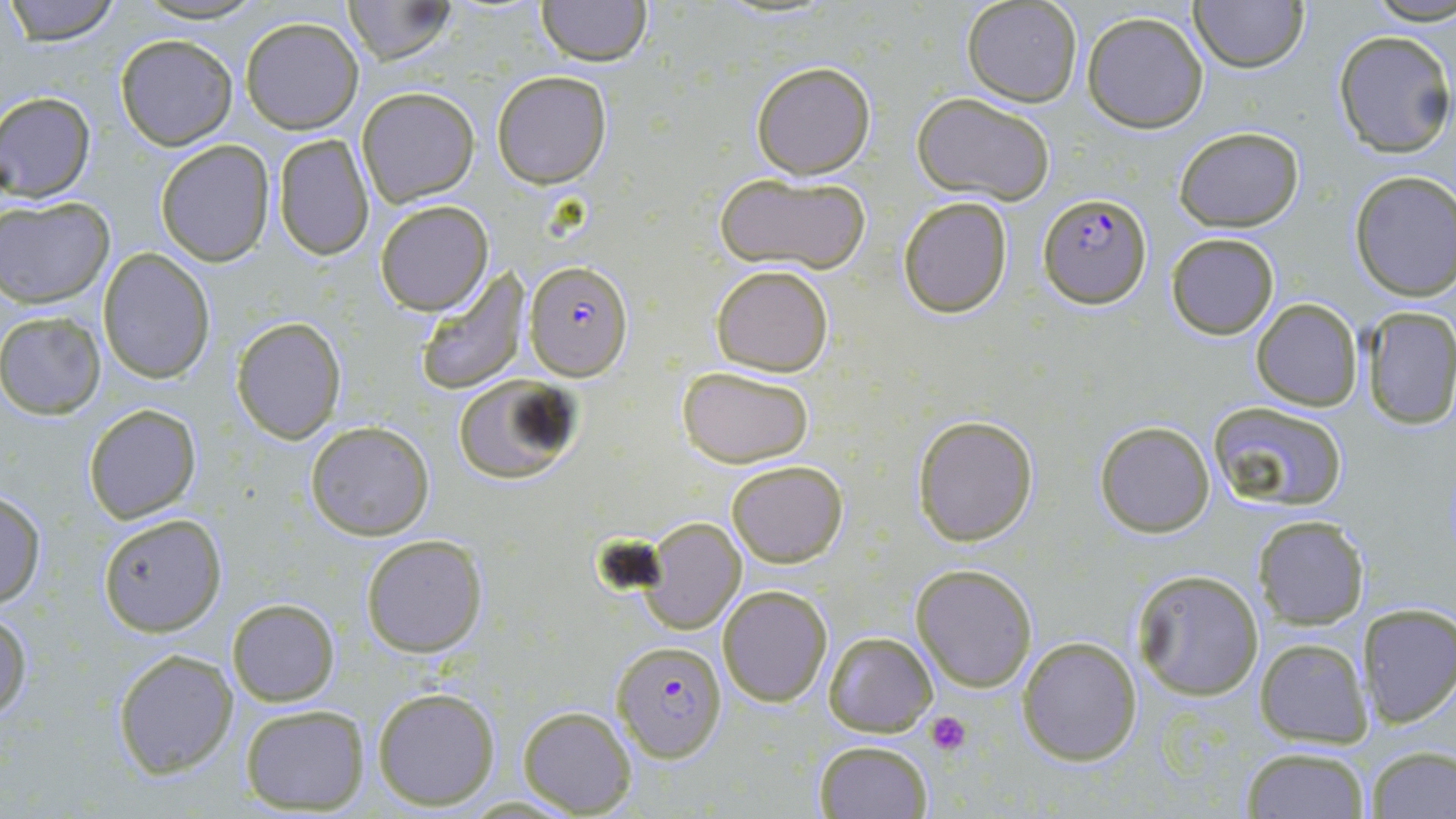

{
  "slide_level_diagnosis": "Plasmodium falciparum",
  "modality": "light microscopy",
  "field_of_view": "single",
  "stain": "May-Grünwald-Giemsa",
  "uninfected_red_blood_cell_locations": "approximate bounding boxes as named x1/y1/x2/y2 corners in pixels: (x1=5, y1=0, x2=121, y2=45), (x1=130, y1=0, x2=268, y2=24), (x1=341, y1=0, x2=461, y2=65), (x1=533, y1=0, x2=652, y2=66), (x1=1189, y1=0, x2=1308, y2=73), (x1=1369, y1=0, x2=1455, y2=27), (x1=962, y1=1, x2=1084, y2=107), (x1=1082, y1=10, x2=1210, y2=133), (x1=240, y1=17, x2=364, y2=133), (x1=1331, y1=28, x2=1456, y2=157), (x1=114, y1=33, x2=239, y2=150), (x1=750, y1=61, x2=876, y2=180), (x1=491, y1=70, x2=613, y2=189), (x1=356, y1=87, x2=480, y2=207), (x1=1, y1=91, x2=96, y2=200), (x1=911, y1=91, x2=1058, y2=204), (x1=1174, y1=126, x2=1305, y2=232), (x1=271, y1=133, x2=375, y2=262), (x1=155, y1=139, x2=275, y2=267), (x1=712, y1=170, x2=871, y2=276), (x1=1347, y1=170, x2=1456, y2=301), (x1=1, y1=197, x2=115, y2=307), (x1=897, y1=197, x2=1014, y2=319), (x1=374, y1=200, x2=493, y2=316), (x1=1165, y1=232, x2=1279, y2=340), (x1=96, y1=249, x2=214, y2=382), (x1=413, y1=263, x2=527, y2=394), (x1=711, y1=263, x2=834, y2=376), (x1=1251, y1=298, x2=1361, y2=410), (x1=1359, y1=309, x2=1456, y2=429), (x1=0, y1=311, x2=105, y2=420), (x1=231, y1=316, x2=347, y2=443), (x1=678, y1=365, x2=816, y2=468), (x1=449, y1=373, x2=582, y2=486), (x1=1206, y1=400, x2=1350, y2=511), (x1=83, y1=404, x2=201, y2=523), (x1=911, y1=413, x2=1040, y2=547), (x1=304, y1=420, x2=435, y2=540), (x1=1095, y1=420, x2=1215, y2=537), (x1=726, y1=460, x2=848, y2=568), (x1=0, y1=489, x2=47, y2=610), (x1=98, y1=513, x2=226, y2=637), (x1=1255, y1=516, x2=1370, y2=629), (x1=640, y1=517, x2=747, y2=634), (x1=360, y1=534, x2=489, y2=658), (x1=911, y1=564, x2=1038, y2=692), (x1=1130, y1=567, x2=1266, y2=700), (x1=717, y1=585, x2=832, y2=705), (x1=227, y1=598, x2=340, y2=708), (x1=1357, y1=602, x2=1456, y2=728), (x1=0, y1=611, x2=31, y2=723), (x1=823, y1=631, x2=936, y2=736), (x1=1017, y1=636, x2=1142, y2=766), (x1=1256, y1=637, x2=1373, y2=748), (x1=112, y1=648, x2=238, y2=777), (x1=372, y1=687, x2=500, y2=810), (x1=240, y1=705, x2=369, y2=812), (x1=517, y1=705, x2=636, y2=816), (x1=812, y1=741, x2=933, y2=819), (x1=1367, y1=746, x2=1455, y2=818), (x1=1240, y1=747, x2=1372, y2=818)",
  "image_size": "1456×819 pixels",
  "magnification": "1000x",
  "preparation": "thin blood film",
  "plasmodium_falciparum_infected_red_blood_cell_locations": "approximate bounding boxes as named x1/y1/x2/y2 corners in pixels: (x1=1038, y1=192, x2=1153, y2=308), (x1=525, y1=260, x2=634, y2=380), (x1=611, y1=640, x2=728, y2=760)",
  "platelet_locations": "approximate bounding boxes as named x1/y1/x2/y2 corners in pixels: (x1=927, y1=711, x2=970, y2=756)"
}